Report the malaria status of this cell.
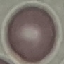

It is uninfected.

preparation = thin blood film
capture = smartphone through the microscope eyepiece
stain = Giemsa
image type = automatically extracted cell patch, resized to 64 × 64 pixels